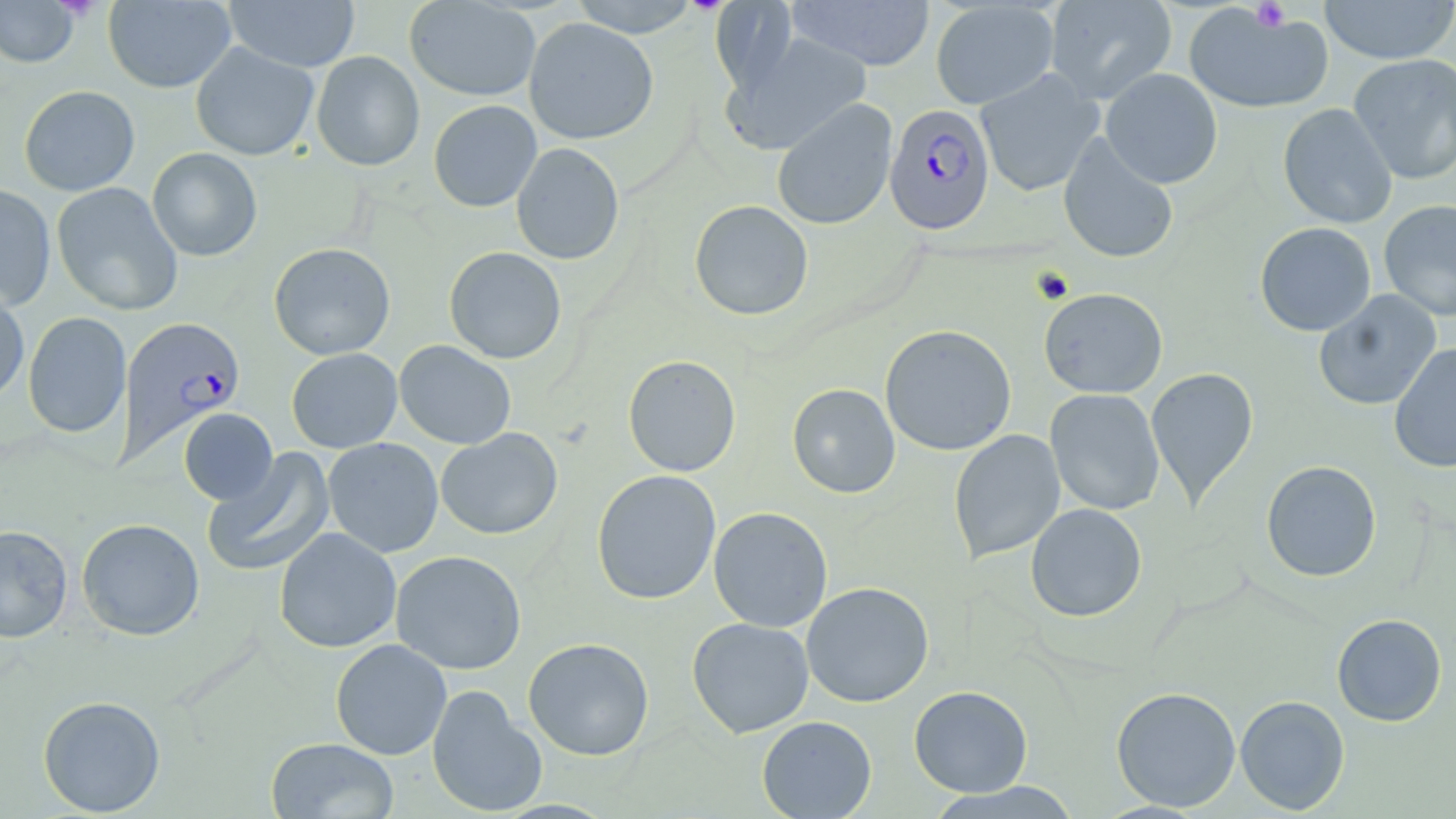

slide-level diagnosis = Plasmodium falciparum
modality = optical microscopy
stain = May-Grünwald-Giemsa
preparation = thin blood smear
Plasmodium falciparum-infected red blood cell locations = approximate bounding boxes as (x1,y1)-(x2,y2) corner pairs in pixels: (884,103)-(995,235), (117,316)-(246,463)
platelet locations = approximate bounding boxes as (x1,y1)-(x2,y2) corner pairs in pixels: (1249,1)-(1290,31)
magnification = 1000x
field of view = one of a larger specimen
uninfected red blood cell locations = approximate bounding boxes as (x1,y1)-(x2,y2) corner pairs in pixels: (567,0)-(702,37), (785,0)-(935,71), (1044,0)-(1177,104), (1319,0)-(1456,65), (0,1)-(80,68), (103,1)-(236,93), (224,1)-(360,72), (404,1)-(541,102), (930,1)-(1059,109), (1182,3)-(1334,115), (524,17)-(659,145), (721,31)-(872,155), (190,42)-(319,160), (311,51)-(425,171), (1348,54)-(1456,185), (1100,68)-(1223,188), (975,69)-(1104,197), (19,85)-(140,196), (771,99)-(898,231), (428,100)-(542,212), (1278,103)-(1397,229), (1058,134)-(1179,264), (511,142)-(625,265), (146,147)-(262,261), (51,182)-(183,316), (0,183)-(56,311), (1378,199)-(1456,322), (689,200)-(814,321), (1254,222)-(1376,336), (269,242)-(396,360), (444,246)-(567,364), (0,286)-(29,405), (1039,287)-(1168,399), (1313,290)-(1442,410), (1355,309)-(1452,453), (23,311)-(132,438), (880,324)-(1017,456), (394,340)-(516,450), (1388,343)-(1456,473), (286,348)-(402,453), (623,354)-(741,477), (1146,367)-(1259,508), (787,383)-(900,499), (1045,388)-(1165,515), (179,408)-(278,505), (435,428)-(563,540), (948,429)-(1065,564), (323,437)-(444,558), (201,446)-(336,579), (1261,460)-(1382,582), (591,469)-(721,604), (1025,503)-(1147,622), (708,507)-(833,633), (76,518)-(205,641), (0,524)-(73,643), (274,527)-(402,653), (390,550)-(527,675), (801,582)-(934,708), (1332,613)-(1447,726), (687,617)-(814,738), (523,637)-(655,761), (330,639)-(452,760), (426,685)-(547,817), (909,685)-(1033,797), (1111,686)-(1241,811), (37,695)-(166,816), (1235,695)-(1350,814), (757,715)-(877,818), (265,737)-(398,818), (923,782)-(1084,818)
image size = 1456×819 pixels